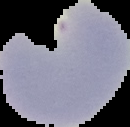

image size = 130×127 pixels
preparation = thin blood smear
result = Plasmodium parasites detected
image type = cell region segmented out of the field of view; surrounding area masked to black